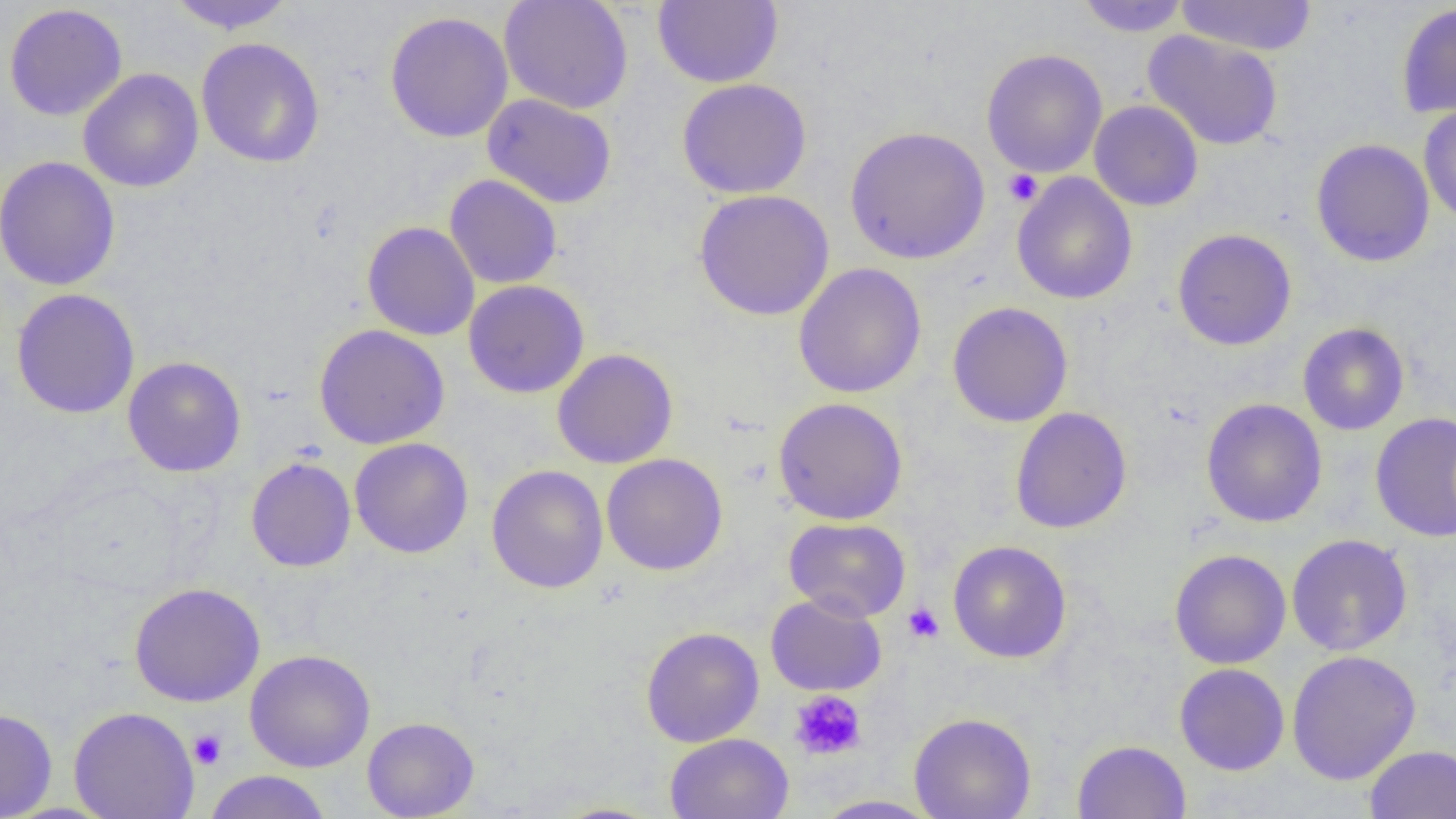

{
  "slide_level_diagnosis": "no evidence of blood parasites",
  "uninfected_red_blood_cell_locations": "approximate bounding boxes as (x1,y1)-(x2,y2) corner pairs in pixels: (166,0)-(297,34), (499,0)-(633,114), (653,0)-(783,88), (1076,0)-(1192,37), (1175,0)-(1318,56), (1396,2)-(1456,119), (4,4)-(128,121), (384,11)-(514,143), (1142,31)-(1284,151), (196,37)-(325,168), (981,48)-(1108,178), (78,68)-(204,193), (676,78)-(812,199), (482,93)-(617,208), (1089,99)-(1203,211), (1418,103)-(1456,226), (845,125)-(990,265), (1311,138)-(1435,267), (1,156)-(120,291), (1011,173)-(1138,305), (444,174)-(562,289), (694,189)-(834,321), (362,221)-(480,341), (1172,228)-(1297,351), (793,263)-(927,398), (463,279)-(590,398), (11,288)-(140,419), (947,301)-(1073,427), (1297,323)-(1410,435), (313,324)-(450,449), (552,348)-(678,469), (122,356)-(247,477), (773,397)-(908,525), (1201,398)-(1327,528), (1010,407)-(1132,533), (1370,412)-(1456,543), (349,438)-(474,558), (602,453)-(728,575), (245,457)-(357,572), (486,464)-(609,593), (784,517)-(911,622), (1286,534)-(1413,656), (948,540)-(1072,663), (1169,549)-(1291,669), (128,582)-(266,707), (765,593)-(887,696), (641,626)-(764,748), (245,649)-(376,772), (1286,650)-(1421,785), (1174,663)-(1290,775), (68,706)-(199,819), (0,707)-(58,818), (908,712)-(1037,819), (362,716)-(479,819), (664,732)-(794,819), (1072,739)-(1191,819), (1363,745)-(1456,819), (202,770)-(333,819), (812,794)-(943,818), (549,802)-(666,819)",
  "field_of_view": "one of a larger specimen",
  "image_size": "1456×819 pixels",
  "preparation": "thin blood smear",
  "platelet_locations": "approximate bounding boxes as (x1,y1)-(x2,y2) corner pairs in pixels: (1003,169)-(1043,206), (903,602)-(945,643), (789,690)-(866,761), (188,729)-(228,769)",
  "modality": "light microscopy",
  "magnification": "1000x"
}